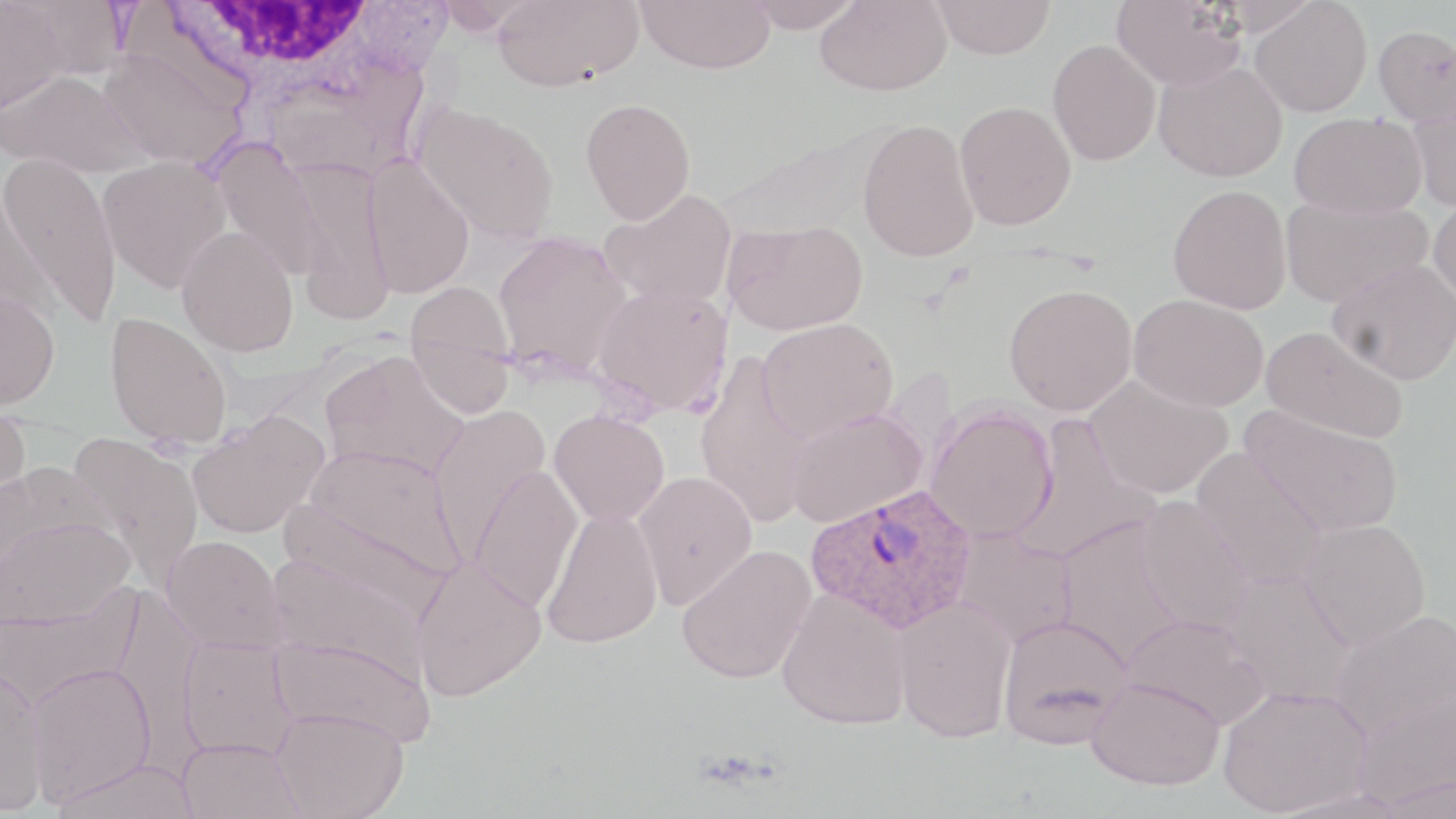
Approximate bounding boxes as named x1/y1/x2/y2 corners in pixels. Plasmodium ovale-infected red blood cell locations: (x1=807, y1=483, x2=976, y2=634). Uninfected red blood cell locations: (x1=0, y1=0, x2=70, y2=115), (x1=8, y1=0, x2=128, y2=80), (x1=432, y1=0, x2=544, y2=35), (x1=493, y1=0, x2=643, y2=92), (x1=636, y1=0, x2=775, y2=74), (x1=743, y1=0, x2=862, y2=32), (x1=931, y1=0, x2=1056, y2=59), (x1=1112, y1=0, x2=1246, y2=90), (x1=815, y1=1, x2=952, y2=96), (x1=1249, y1=1, x2=1372, y2=117), (x1=1373, y1=25, x2=1455, y2=126), (x1=1048, y1=39, x2=1161, y2=167), (x1=97, y1=47, x2=245, y2=171), (x1=1153, y1=61, x2=1287, y2=182), (x1=1, y1=69, x2=149, y2=179), (x1=1407, y1=97, x2=1456, y2=213), (x1=580, y1=98, x2=696, y2=225), (x1=410, y1=101, x2=561, y2=244), (x1=954, y1=101, x2=1076, y2=231), (x1=1289, y1=112, x2=1426, y2=219), (x1=857, y1=118, x2=980, y2=263), (x1=210, y1=138, x2=326, y2=282), (x1=1, y1=153, x2=124, y2=327), (x1=361, y1=155, x2=475, y2=299), (x1=98, y1=156, x2=231, y2=294), (x1=290, y1=159, x2=395, y2=325), (x1=0, y1=182, x2=52, y2=325), (x1=1168, y1=184, x2=1292, y2=314), (x1=600, y1=188, x2=737, y2=309), (x1=1428, y1=194, x2=1456, y2=310), (x1=1279, y1=195, x2=1432, y2=307), (x1=723, y1=218, x2=868, y2=336), (x1=177, y1=226, x2=299, y2=356), (x1=493, y1=230, x2=632, y2=375), (x1=1327, y1=258, x2=1456, y2=384), (x1=405, y1=282, x2=515, y2=412), (x1=1003, y1=283, x2=1138, y2=415), (x1=592, y1=284, x2=733, y2=416), (x1=0, y1=287, x2=60, y2=410), (x1=1129, y1=294, x2=1269, y2=412), (x1=105, y1=312, x2=232, y2=448), (x1=757, y1=317, x2=898, y2=442), (x1=1260, y1=325, x2=1410, y2=444), (x1=319, y1=351, x2=469, y2=482), (x1=694, y1=354, x2=816, y2=526), (x1=1084, y1=374, x2=1233, y2=499), (x1=0, y1=398, x2=31, y2=520), (x1=428, y1=404, x2=552, y2=552), (x1=1240, y1=405, x2=1403, y2=539), (x1=925, y1=406, x2=1058, y2=543), (x1=786, y1=407, x2=926, y2=528), (x1=549, y1=409, x2=670, y2=526), (x1=188, y1=411, x2=330, y2=539), (x1=1009, y1=415, x2=1160, y2=564), (x1=67, y1=432, x2=205, y2=588), (x1=299, y1=445, x2=465, y2=584), (x1=1191, y1=449, x2=1328, y2=590), (x1=468, y1=465, x2=583, y2=612), (x1=632, y1=471, x2=757, y2=610), (x1=1135, y1=497, x2=1256, y2=635), (x1=281, y1=500, x2=449, y2=624), (x1=541, y1=508, x2=663, y2=649), (x1=1, y1=516, x2=135, y2=632), (x1=1055, y1=518, x2=1185, y2=665), (x1=1298, y1=518, x2=1431, y2=651), (x1=953, y1=528, x2=1077, y2=648), (x1=162, y1=535, x2=287, y2=653), (x1=676, y1=545, x2=816, y2=684), (x1=266, y1=551, x2=432, y2=682), (x1=410, y1=557, x2=547, y2=700), (x1=1223, y1=569, x2=1358, y2=708), (x1=0, y1=588, x2=142, y2=711), (x1=776, y1=589, x2=911, y2=730), (x1=892, y1=597, x2=1016, y2=743), (x1=1328, y1=610, x2=1456, y2=742), (x1=997, y1=613, x2=1134, y2=748), (x1=1120, y1=613, x2=1268, y2=729), (x1=269, y1=635, x2=436, y2=746), (x1=178, y1=637, x2=298, y2=762), (x1=25, y1=663, x2=156, y2=807), (x1=0, y1=664, x2=50, y2=816), (x1=1086, y1=673, x2=1226, y2=790), (x1=1218, y1=684, x2=1372, y2=816), (x1=1353, y1=688, x2=1456, y2=811), (x1=272, y1=708, x2=408, y2=819), (x1=176, y1=737, x2=307, y2=819), (x1=52, y1=757, x2=200, y2=819). White blood cell locations: (x1=146, y1=1, x2=420, y2=100). Slide-level diagnosis: Plasmodium ovale. Thin blood smear. May-Grünwald-Giemsa-stained preparation. Optical microscopy. Single field of view. 1000x magnification. Image is 1456×819 pixels.